Give the extent of all Plasmodium ovale-infected red blood cells.
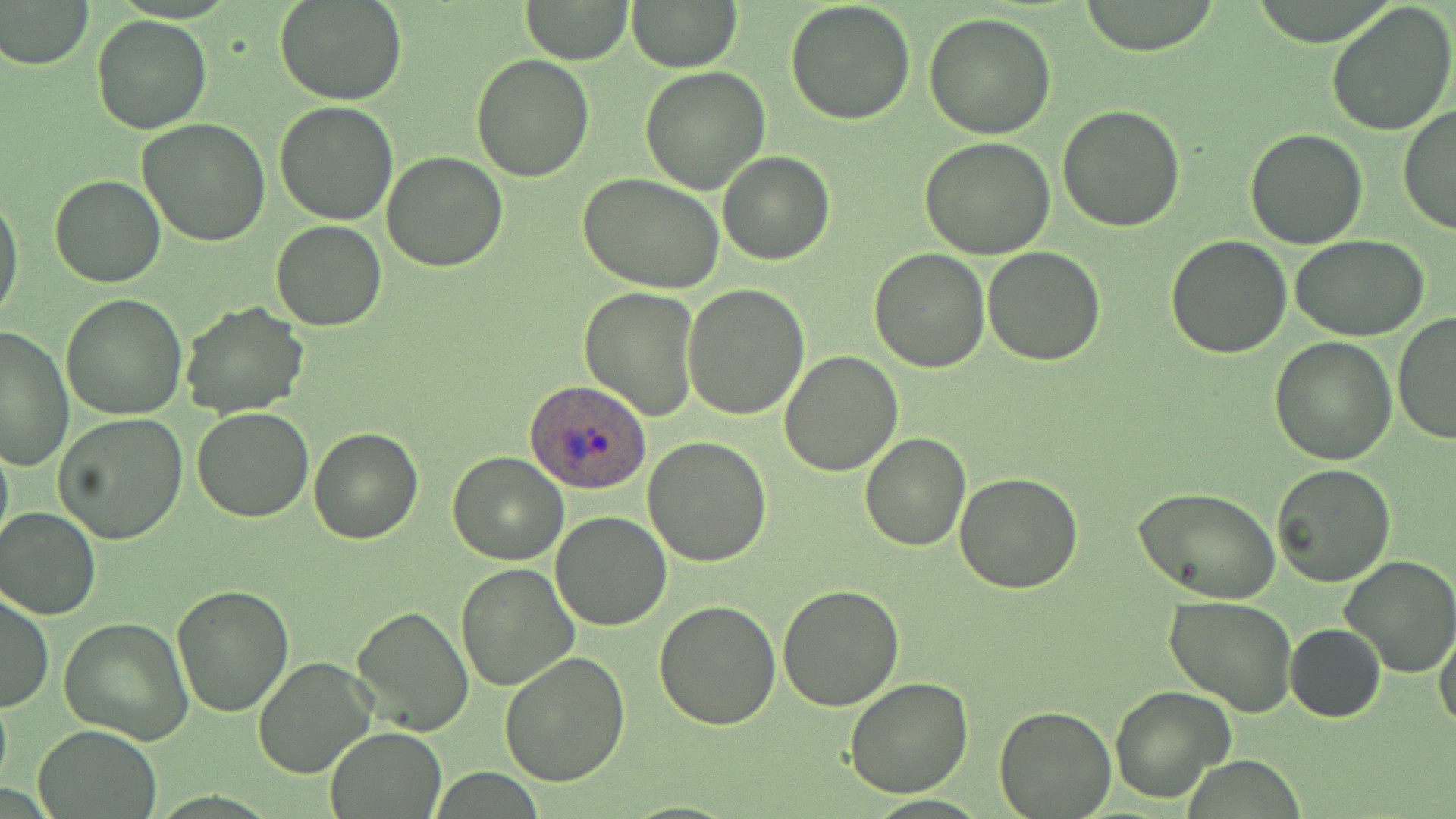

Approximate bounding boxes as [x1, y1, x2, y2] in pixels.
Plasmodium ovale-infected red blood cells: [526, 380, 651, 495].

{
  "slide_level_diagnosis": "Plasmodium ovale",
  "stain": "May-Grünwald-Giemsa",
  "field_of_view": "one of a larger specimen",
  "preparation": "thin blood smear",
  "image_size": "1456×819 pixels",
  "magnification": "1000x",
  "uninfected_red_blood_cell_locations": "approximate bounding boxes as [x1, y1, x2, y2] in pixels: [276, 0, 406, 105], [520, 0, 633, 65], [786, 0, 915, 123], [1077, 0, 1224, 55], [2, 1, 92, 69], [1327, 1, 1456, 138], [629, 2, 740, 71], [923, 11, 1059, 138], [92, 14, 212, 134], [471, 53, 595, 182], [639, 65, 770, 194], [274, 101, 397, 225], [1397, 102, 1456, 235], [1058, 103, 1186, 230], [139, 118, 271, 246], [1243, 126, 1368, 248], [920, 137, 1058, 259], [716, 150, 835, 265], [382, 152, 508, 272], [49, 174, 166, 289], [580, 174, 725, 294], [0, 190, 24, 326], [270, 220, 387, 331], [1166, 234, 1292, 357], [1292, 236, 1428, 342], [868, 247, 992, 371], [983, 247, 1105, 366], [683, 284, 811, 418], [578, 287, 700, 421], [60, 293, 189, 420], [180, 301, 310, 419], [1393, 311, 1456, 445], [0, 325, 74, 471], [1270, 336, 1399, 465], [779, 349, 903, 477], [192, 407, 314, 523], [53, 410, 189, 544], [309, 426, 423, 544], [861, 431, 969, 549], [0, 434, 13, 560], [644, 437, 771, 566], [446, 451, 568, 565], [1270, 462, 1399, 587], [953, 472, 1083, 593], [1139, 472, 1395, 590], [1137, 490, 1280, 605], [0, 507, 100, 620], [550, 509, 672, 629], [1338, 555, 1455, 677], [457, 561, 581, 691], [171, 584, 294, 717], [777, 584, 903, 710], [0, 593, 53, 712], [1164, 597, 1297, 716], [655, 600, 781, 730], [351, 605, 474, 734], [59, 617, 193, 744], [1284, 623, 1386, 722], [1433, 627, 1456, 735], [499, 652, 630, 787], [252, 654, 377, 778], [844, 675, 974, 797], [1108, 685, 1235, 805], [0, 686, 12, 799], [993, 705, 1116, 818], [33, 726, 159, 819], [325, 727, 444, 817]",
  "modality": "optical microscopy"
}